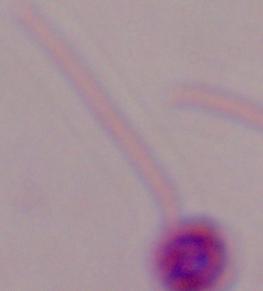

1000x magnification. Photomicrograph. A Leishmania parasite is shown.